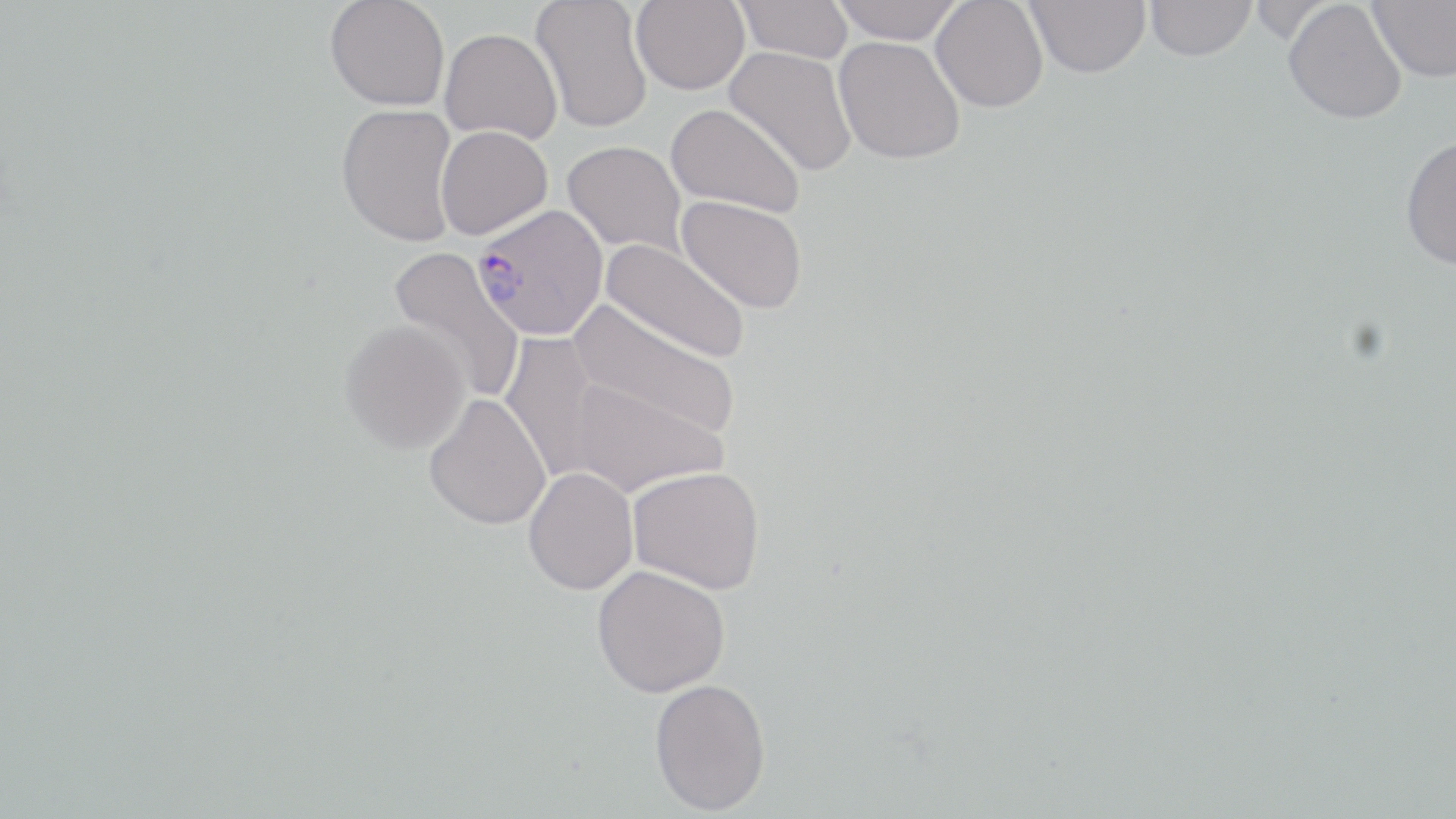

Approximate bounding boxes as (x1, y1, x2, y2) in pixels. Uninfected red blood cell locations: (325, 0, 450, 111), (530, 0, 654, 134), (631, 0, 750, 95), (735, 0, 853, 63), (831, 0, 964, 44), (931, 0, 1049, 113), (1025, 0, 1151, 78), (1247, 0, 1338, 44), (1367, 0, 1456, 83), (1146, 1, 1256, 61), (1283, 1, 1407, 124), (439, 28, 562, 144), (833, 36, 965, 165), (724, 46, 857, 176), (336, 103, 460, 247), (666, 103, 805, 217), (436, 125, 553, 240), (1400, 135, 1456, 271), (562, 141, 687, 253), (676, 194, 808, 313), (600, 239, 750, 364), (389, 246, 526, 403), (573, 302, 741, 439), (340, 320, 471, 453), (499, 331, 607, 483), (565, 374, 726, 497), (423, 392, 552, 530), (628, 466, 766, 593), (523, 467, 639, 595), (592, 565, 731, 697), (649, 678, 771, 815). Plasmodium vivax-infected red blood cell locations: (472, 204, 608, 340). Slide-level diagnosis: Plasmodium vivax. Single field of view. Thin blood film. Captured at 1000x magnification. May-Grünwald-Giemsa-stained preparation. Optical microscopy. Image is 1456×819 pixels.